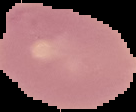
Summary:
  - Preparation: thin blood smear
  - Image type: segmented cell region on a black background
  - Malaria status: uninfected
  - Image size: 136×112 pixels